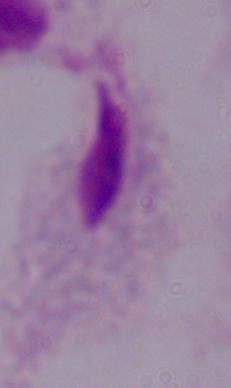

1000x magnification. Micrograph. A trichomonad is shown.